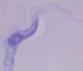
Summary:
  - Modality: micrograph
  - Identification: trypanosome
  - Magnification: 1000x